State which parasite is depicted.
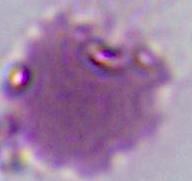

This is Plasmodium.

Summary:
  - Magnification: 400x or 1000x
  - Modality: micrograph